Locate every blood parasite and identify its species.
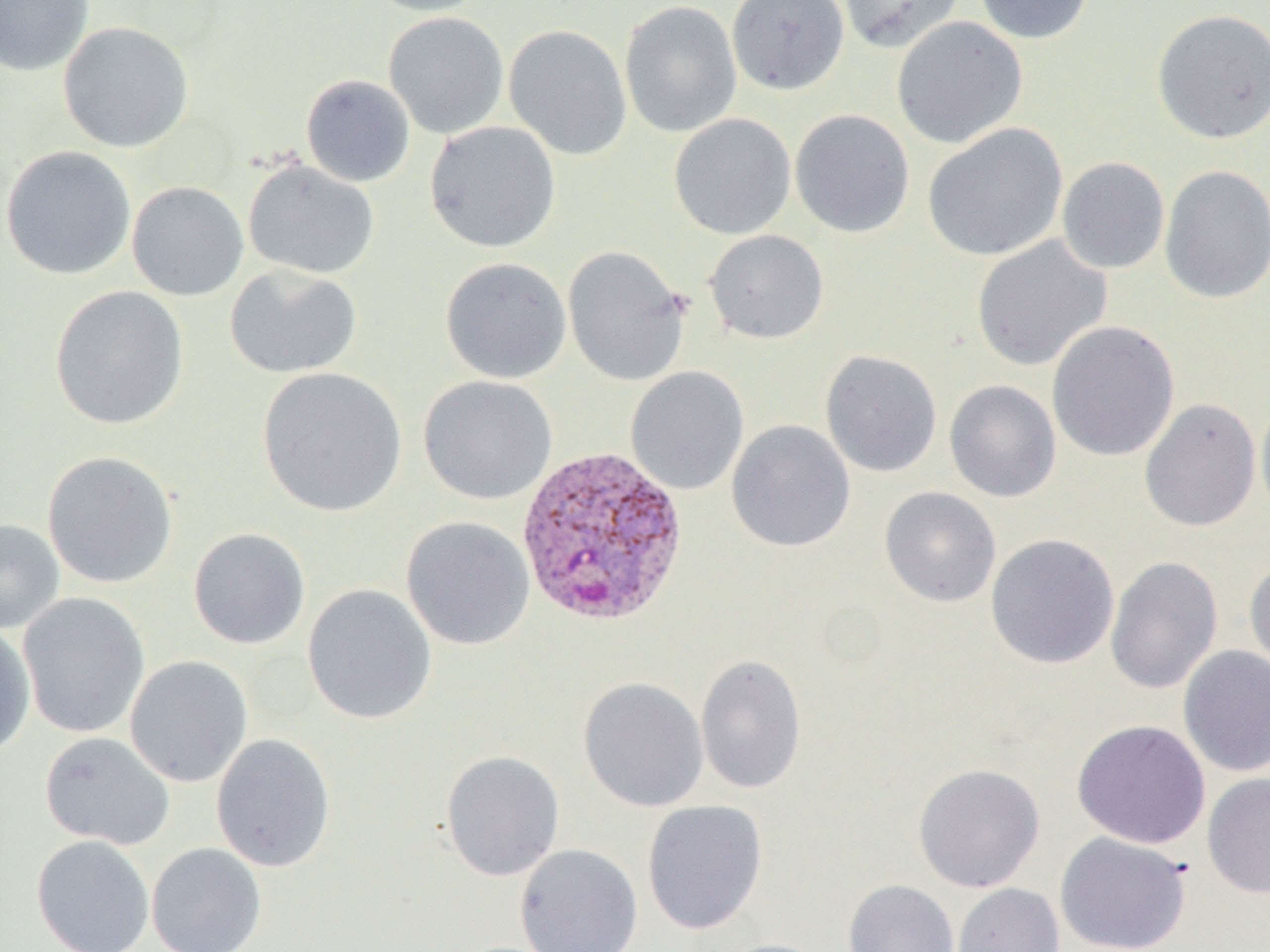
Approximate bounding boxes as named x1/y1/x2/y2 corners in pixels.
Plasmodium vivax-infected red blood cells: (x1=515, y1=444, x2=689, y2=626).
No Plasmodium falciparum, Plasmodium ovale, Plasmodium malariae, Babesia divergens, or Trypanosoma brucei observed.

{
  "slide_level_diagnosis": "Plasmodium vivax",
  "modality": "light microscopy",
  "image_size": "1270×952 pixels",
  "magnification": "1000x",
  "field_of_view": "single",
  "preparation": "thin blood smear",
  "uninfected_red_blood_cell_locations": "approximate bounding boxes as named x1/y1/x2/y2 corners in pixels: (x1=0, y1=0, x2=94, y2=76), (x1=365, y1=0, x2=494, y2=17), (x1=619, y1=0, x2=742, y2=138), (x1=726, y1=0, x2=850, y2=95), (x1=837, y1=0, x2=966, y2=53), (x1=974, y1=0, x2=1094, y2=45), (x1=1151, y1=9, x2=1270, y2=145), (x1=383, y1=12, x2=509, y2=139), (x1=891, y1=16, x2=1028, y2=148), (x1=57, y1=21, x2=195, y2=153), (x1=503, y1=24, x2=632, y2=161), (x1=301, y1=74, x2=416, y2=187), (x1=790, y1=109, x2=915, y2=238), (x1=668, y1=112, x2=797, y2=240), (x1=424, y1=121, x2=561, y2=253), (x1=922, y1=122, x2=1068, y2=261), (x1=1, y1=146, x2=136, y2=280), (x1=1057, y1=157, x2=1170, y2=274), (x1=243, y1=160, x2=380, y2=279), (x1=1159, y1=164, x2=1270, y2=303), (x1=127, y1=181, x2=249, y2=301), (x1=704, y1=229, x2=829, y2=345), (x1=971, y1=235, x2=1112, y2=371), (x1=563, y1=245, x2=691, y2=387), (x1=440, y1=257, x2=572, y2=384), (x1=224, y1=265, x2=362, y2=379), (x1=49, y1=285, x2=190, y2=430), (x1=1047, y1=321, x2=1180, y2=462), (x1=820, y1=349, x2=942, y2=477), (x1=256, y1=367, x2=407, y2=517), (x1=625, y1=367, x2=749, y2=495), (x1=418, y1=375, x2=557, y2=505), (x1=944, y1=379, x2=1062, y2=503), (x1=1139, y1=398, x2=1261, y2=532), (x1=1255, y1=400, x2=1270, y2=522), (x1=725, y1=420, x2=856, y2=553), (x1=41, y1=451, x2=178, y2=589), (x1=879, y1=486, x2=1001, y2=607), (x1=400, y1=516, x2=535, y2=650), (x1=0, y1=519, x2=65, y2=634), (x1=188, y1=528, x2=311, y2=650), (x1=985, y1=533, x2=1119, y2=669), (x1=1244, y1=555, x2=1270, y2=680), (x1=1105, y1=556, x2=1223, y2=694), (x1=302, y1=584, x2=437, y2=725), (x1=17, y1=592, x2=151, y2=740), (x1=0, y1=622, x2=36, y2=758), (x1=1178, y1=644, x2=1270, y2=777), (x1=695, y1=654, x2=807, y2=795), (x1=124, y1=655, x2=253, y2=787), (x1=578, y1=677, x2=709, y2=813), (x1=1071, y1=719, x2=1211, y2=849), (x1=39, y1=731, x2=174, y2=851), (x1=210, y1=734, x2=336, y2=872), (x1=440, y1=750, x2=565, y2=881), (x1=913, y1=762, x2=1045, y2=893), (x1=1202, y1=772, x2=1270, y2=899), (x1=641, y1=800, x2=768, y2=935), (x1=1055, y1=832, x2=1192, y2=952), (x1=31, y1=835, x2=155, y2=952), (x1=146, y1=842, x2=267, y2=952), (x1=514, y1=843, x2=643, y2=952), (x1=843, y1=879, x2=959, y2=952), (x1=951, y1=883, x2=1065, y2=952), (x1=711, y1=938, x2=835, y2=952)"
}